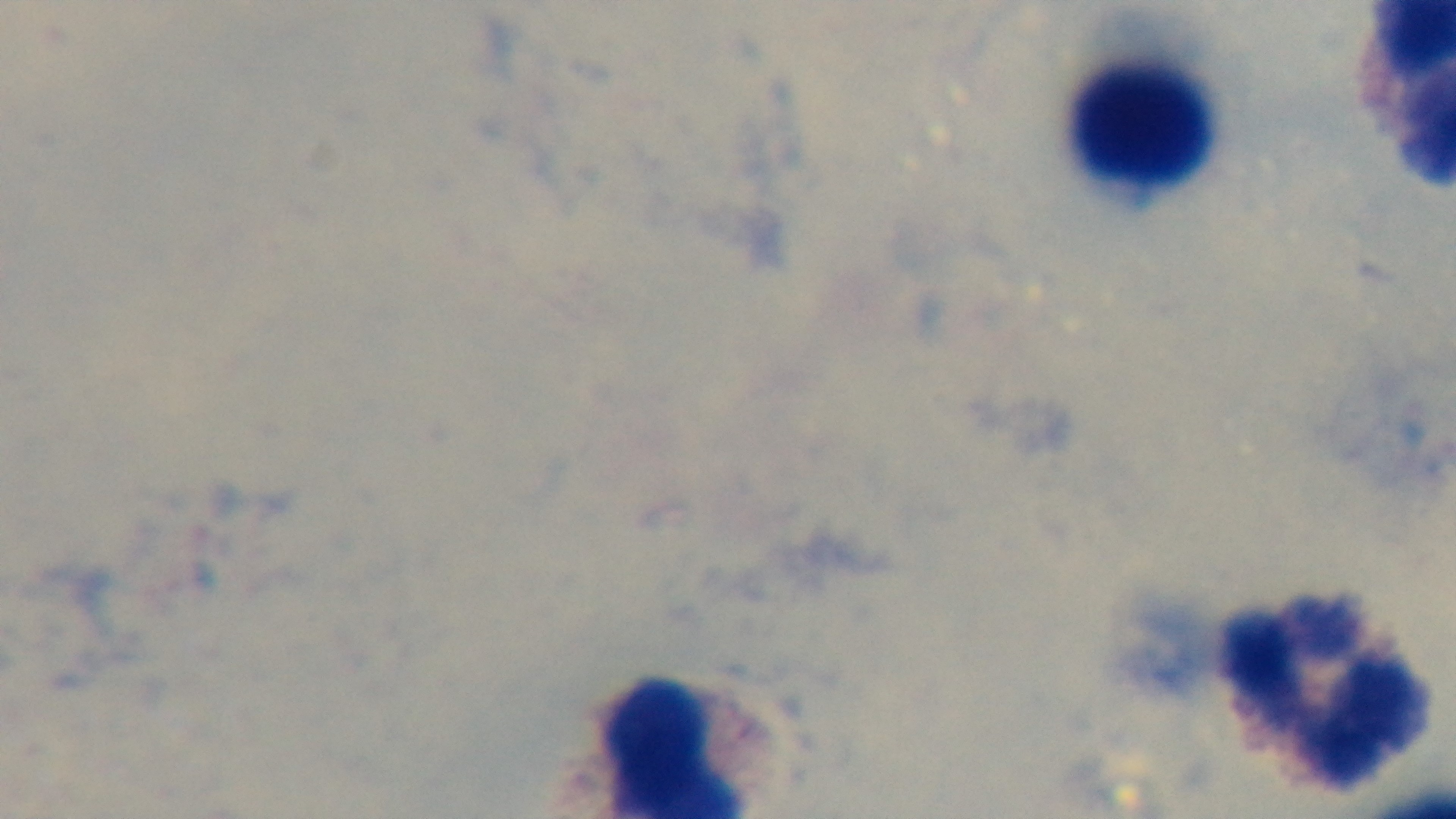

Summary:
  - Capture: mounted 4K digital camera
  - Objective: 100x oil immersion
  - Stain: Giemsa
  - Malaria status: uninfected
  - Modality: light microscopy
  - Field of view: one from the slide
  - Preparation: thick